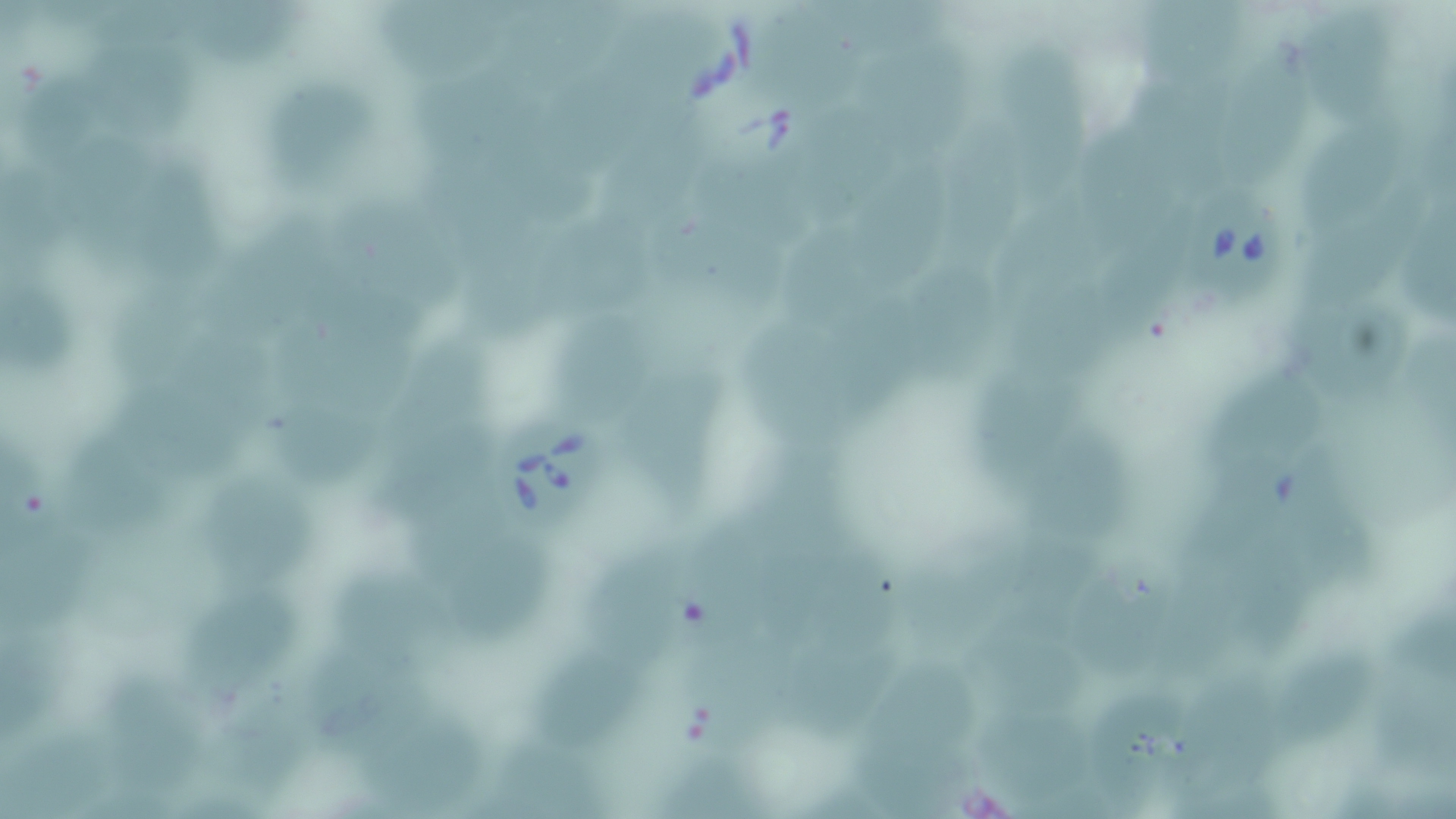 Approximate bounding boxes as named x1/y1/x2/y2 corners in pixels. Uninfected red blood cell locations: (x1=88, y1=0, x2=208, y2=52), (x1=185, y1=0, x2=314, y2=70), (x1=1130, y1=0, x2=1249, y2=92), (x1=747, y1=3, x2=873, y2=109), (x1=379, y1=5, x2=524, y2=96), (x1=507, y1=10, x2=597, y2=119), (x1=1315, y1=14, x2=1401, y2=120), (x1=1011, y1=31, x2=1095, y2=202), (x1=857, y1=34, x2=981, y2=153), (x1=1224, y1=34, x2=1310, y2=183), (x1=100, y1=49, x2=208, y2=141), (x1=414, y1=56, x2=525, y2=144), (x1=556, y1=58, x2=654, y2=174), (x1=1121, y1=58, x2=1236, y2=180), (x1=24, y1=61, x2=113, y2=167), (x1=267, y1=69, x2=381, y2=210), (x1=803, y1=93, x2=901, y2=225), (x1=1300, y1=109, x2=1400, y2=223), (x1=957, y1=113, x2=1036, y2=273), (x1=1093, y1=116, x2=1193, y2=245), (x1=511, y1=124, x2=593, y2=229), (x1=72, y1=128, x2=174, y2=281), (x1=698, y1=129, x2=838, y2=242), (x1=606, y1=135, x2=698, y2=237), (x1=424, y1=136, x2=523, y2=230), (x1=859, y1=143, x2=942, y2=300), (x1=146, y1=155, x2=233, y2=281), (x1=1, y1=157, x2=82, y2=275), (x1=1007, y1=179, x2=1125, y2=278), (x1=650, y1=192, x2=743, y2=305), (x1=1302, y1=195, x2=1429, y2=302), (x1=343, y1=200, x2=473, y2=314), (x1=720, y1=207, x2=790, y2=310), (x1=224, y1=208, x2=343, y2=328), (x1=472, y1=211, x2=567, y2=347), (x1=548, y1=218, x2=662, y2=313), (x1=780, y1=218, x2=878, y2=332), (x1=1105, y1=224, x2=1193, y2=355), (x1=914, y1=263, x2=997, y2=407), (x1=0, y1=267, x2=83, y2=383), (x1=1014, y1=271, x2=1119, y2=368), (x1=118, y1=286, x2=212, y2=400), (x1=1288, y1=296, x2=1422, y2=388), (x1=563, y1=306, x2=660, y2=415), (x1=745, y1=322, x2=881, y2=432), (x1=287, y1=325, x2=397, y2=415), (x1=387, y1=330, x2=492, y2=467), (x1=157, y1=333, x2=260, y2=479), (x1=971, y1=348, x2=1081, y2=483), (x1=618, y1=356, x2=731, y2=523), (x1=1208, y1=364, x2=1349, y2=473), (x1=267, y1=407, x2=387, y2=487), (x1=63, y1=419, x2=172, y2=537), (x1=1035, y1=419, x2=1146, y2=546), (x1=767, y1=420, x2=863, y2=540), (x1=4, y1=442, x2=76, y2=556), (x1=1188, y1=458, x2=1291, y2=580), (x1=1292, y1=459, x2=1398, y2=612), (x1=414, y1=468, x2=509, y2=581), (x1=213, y1=483, x2=324, y2=595), (x1=698, y1=513, x2=795, y2=639), (x1=1, y1=518, x2=96, y2=632), (x1=775, y1=518, x2=913, y2=643), (x1=1023, y1=533, x2=1122, y2=640), (x1=1235, y1=537, x2=1308, y2=670), (x1=595, y1=541, x2=696, y2=652), (x1=898, y1=541, x2=1019, y2=670), (x1=467, y1=550, x2=563, y2=647), (x1=1067, y1=560, x2=1195, y2=672), (x1=343, y1=561, x2=467, y2=656), (x1=192, y1=589, x2=300, y2=695), (x1=991, y1=610, x2=1097, y2=725), (x1=1386, y1=611, x2=1455, y2=678), (x1=678, y1=619, x2=807, y2=749), (x1=787, y1=624, x2=912, y2=738), (x1=534, y1=639, x2=649, y2=737), (x1=306, y1=643, x2=437, y2=753), (x1=1282, y1=645, x2=1386, y2=737), (x1=862, y1=656, x2=983, y2=758), (x1=1181, y1=664, x2=1306, y2=793), (x1=94, y1=671, x2=221, y2=796), (x1=1373, y1=671, x2=1456, y2=777), (x1=218, y1=682, x2=338, y2=794), (x1=1102, y1=686, x2=1184, y2=800), (x1=359, y1=703, x2=493, y2=802), (x1=1, y1=710, x2=137, y2=819), (x1=996, y1=722, x2=1110, y2=808), (x1=488, y1=733, x2=618, y2=813), (x1=859, y1=739, x2=959, y2=819), (x1=657, y1=753, x2=759, y2=818). Babesia divergens-infected red blood cell locations: (x1=1190, y1=187, x2=1288, y2=301), (x1=496, y1=409, x2=611, y2=536). Slide-level diagnosis: Babesia divergens. May-Grünwald-Giemsa-stained preparation. Thin blood film. Image is 1456×819 pixels. Optical microscopy. 1000x magnification. Single field of view.